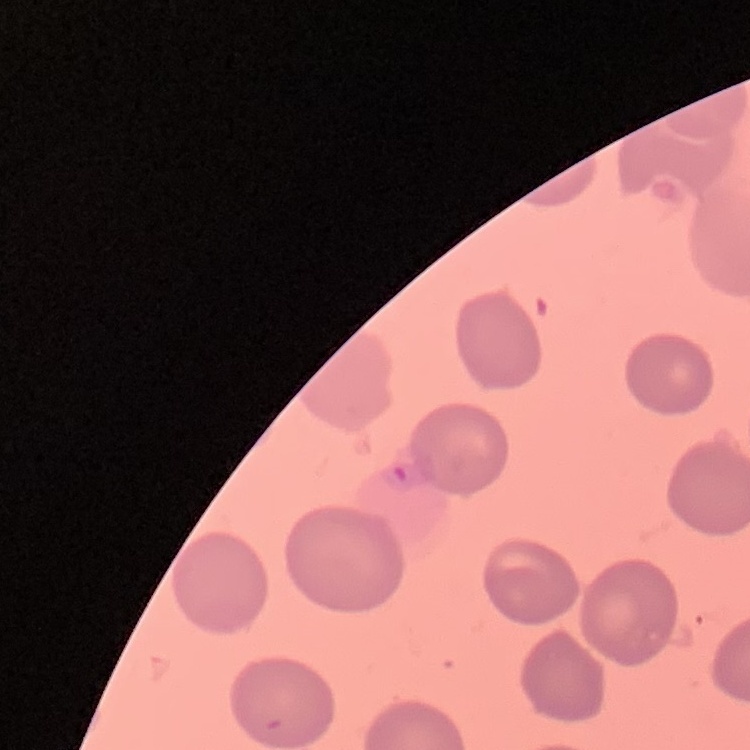

red blood cell morphology = no rouleaux formation
stain = Field's or Giemsa
image type = square crop of a larger photomicrograph
preparation = thin blood film